Assess this cell for malaria.
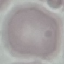
It is uninfected.

Summary:
  - Preparation: thin smear
  - Image type: cell patch, automatically extracted from a larger field of view and resized to 64 × 64 pixels
  - Capture: smartphone camera at the microscope eyepiece
  - Stain: Giemsa